Name the parasite shown.
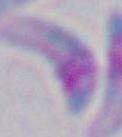
This is Toxoplasma gondii.

{
  "magnification": "1000x",
  "modality": "photomicrograph"
}